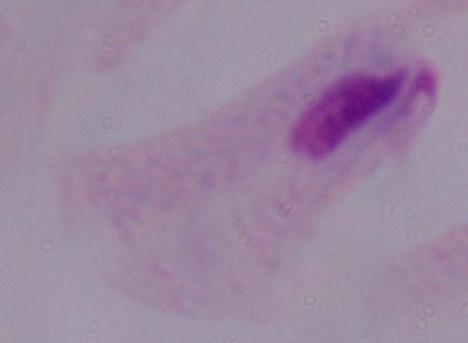 A trichomonad is shown. 1000x magnification. Photomicrograph.